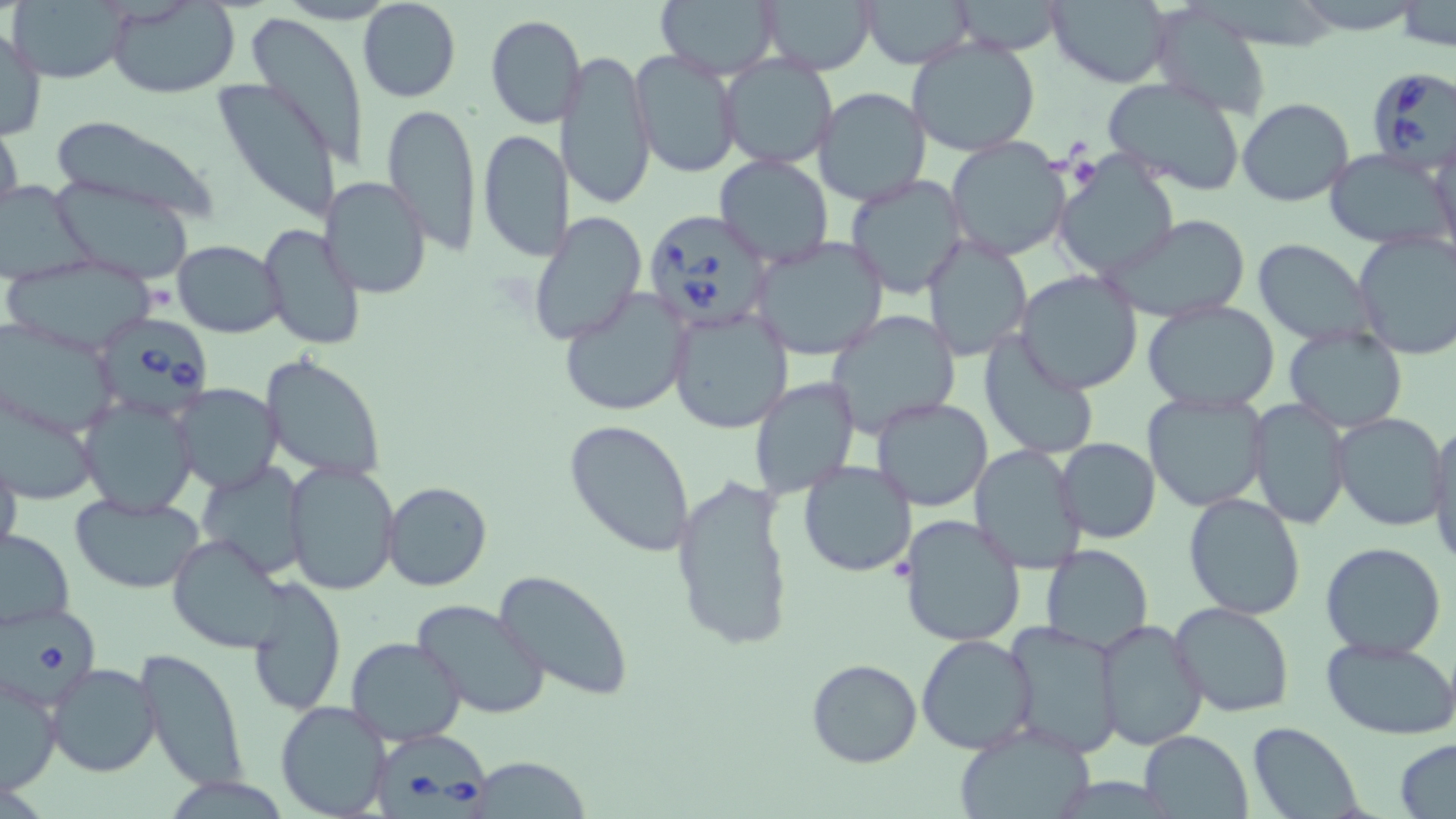

Approximate bounding boxes as (x1, y1, x2, y2) in pixels. Babesia divergens-infected red blood cell locations: (1363, 68, 1456, 170), (643, 209, 775, 334), (92, 311, 215, 419), (5, 601, 101, 708), (370, 733, 493, 819). Uninfected red blood cell locations: (9, 0, 129, 84), (357, 0, 461, 103), (652, 0, 781, 81), (759, 0, 880, 75), (860, 0, 975, 68), (1046, 0, 1174, 87), (105, 1, 241, 97), (946, 1, 1068, 55), (1392, 4, 1455, 49), (1149, 6, 1273, 116), (484, 14, 585, 129), (246, 15, 369, 164), (1, 25, 47, 142), (906, 36, 1042, 156), (558, 50, 656, 209), (631, 50, 741, 178), (719, 54, 839, 169), (1100, 75, 1248, 195), (213, 78, 344, 224), (811, 86, 931, 209), (1236, 98, 1354, 207), (381, 101, 483, 252), (44, 115, 223, 223), (0, 117, 23, 227), (477, 130, 571, 262), (945, 137, 1072, 262), (1428, 140, 1456, 263), (1324, 147, 1455, 251), (713, 155, 834, 268), (1054, 155, 1179, 280), (843, 174, 969, 299), (320, 176, 431, 300), (1, 179, 94, 287), (52, 180, 196, 284), (528, 211, 646, 346), (1104, 214, 1255, 324), (256, 223, 368, 353), (1352, 231, 1456, 361), (922, 232, 1033, 361), (750, 236, 889, 360), (171, 240, 285, 337), (1252, 240, 1380, 347), (3, 257, 161, 356), (1014, 271, 1143, 394), (558, 289, 692, 415), (1141, 301, 1282, 414), (667, 304, 794, 434), (827, 311, 962, 437), (2, 319, 121, 440), (1283, 326, 1407, 434), (978, 333, 1102, 460), (260, 352, 386, 482), (750, 376, 859, 499), (173, 383, 281, 493), (1142, 391, 1270, 513), (78, 397, 198, 516), (871, 397, 996, 512), (1248, 399, 1351, 529), (1333, 413, 1449, 530), (564, 419, 695, 555), (1426, 425, 1456, 561), (1056, 437, 1160, 544), (969, 444, 1087, 570), (0, 449, 23, 570), (284, 460, 399, 597), (796, 460, 917, 578), (196, 465, 309, 581), (672, 476, 796, 654), (381, 481, 493, 593), (1184, 492, 1308, 621), (70, 493, 205, 595), (898, 512, 1027, 649), (0, 528, 75, 630), (167, 533, 294, 655), (1319, 541, 1448, 659), (1041, 544, 1153, 656), (493, 569, 634, 700), (246, 575, 347, 718), (412, 597, 551, 721), (1167, 602, 1295, 717), (1097, 617, 1210, 751), (1002, 621, 1125, 759), (916, 632, 1038, 753), (346, 636, 467, 745), (1321, 637, 1456, 740), (136, 645, 249, 791), (805, 659, 924, 768), (45, 662, 161, 777), (2, 673, 61, 794), (276, 701, 392, 819), (1247, 722, 1364, 819), (952, 723, 1099, 818), (1137, 731, 1253, 817), (1395, 738, 1456, 817), (478, 763, 595, 819). Slide-level diagnosis: Babesia divergens. Light microscopy. Single field of view. May-Grünwald-Giemsa stain. Image is 1456×819 pixels. Thin blood smear. 1000x magnification.